Classify this cell by malaria status.
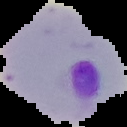

It is parasitized.

Summary:
  - Image type: cell region segmented out of the field of view; surrounding area masked to black
  - Image size: 127×127 pixels
  - Preparation: thin blood smear